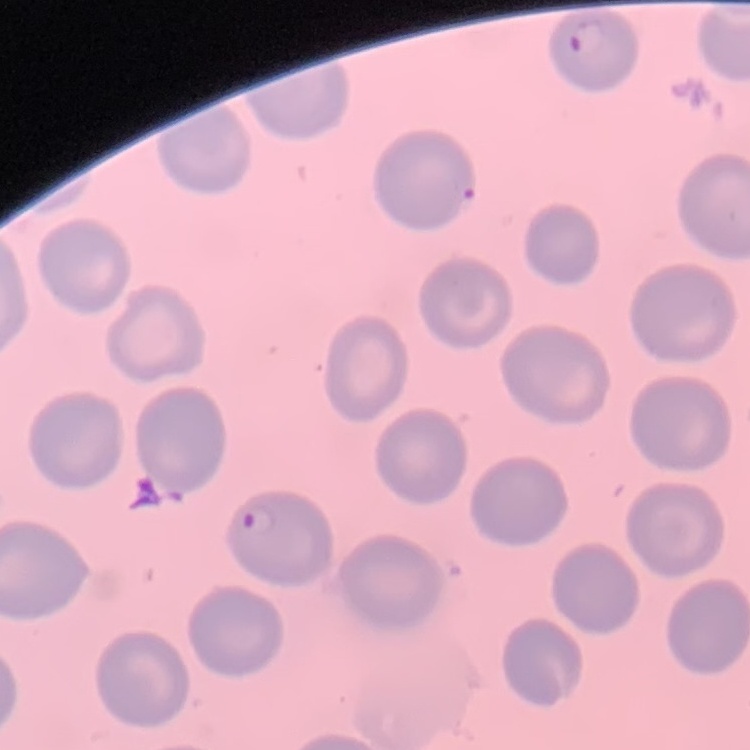

The erythrocytes show no rouleaux formation. Stained with either Field's or Giemsa. Square crop of a larger photomicrograph. Thin peripheral smear.